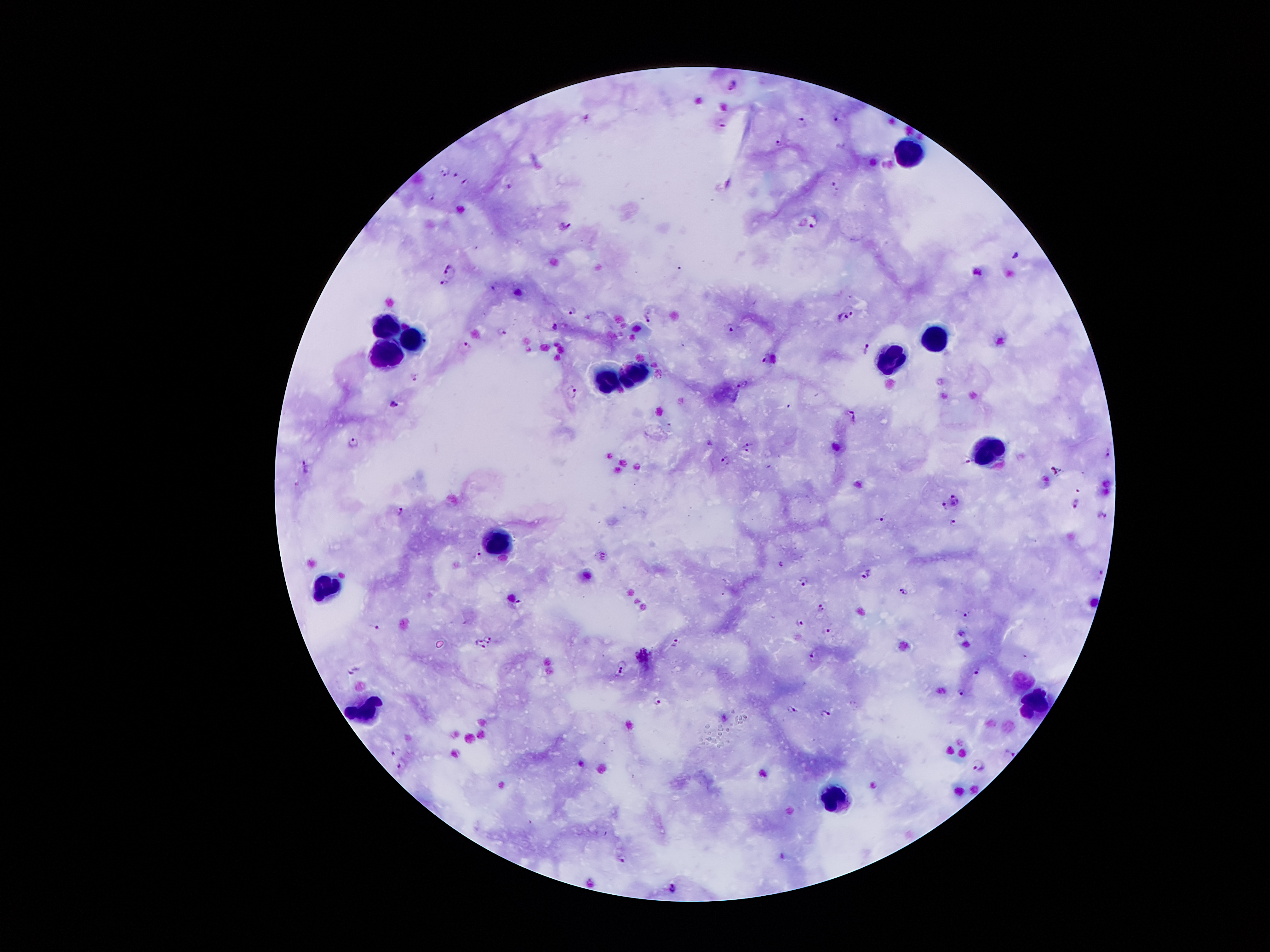
{
  "image_size": "1270×952 pixels",
  "patient_malaria_status": "infected with Plasmodium falciparum",
  "preparation": "thick blood film",
  "magnification": "100x",
  "field_of_view": "single",
  "leukocyte_locations": "approximate centers as [x, y] in pixels: [906, 152], [391, 324], [418, 336], [934, 338], [390, 354], [887, 357], [636, 371], [611, 380], [992, 446], [502, 539], [330, 584], [1023, 680], [1037, 702], [367, 710], [836, 796]",
  "malaria_parasite_locations": "approximate centers as [x, y] in pixels: [734, 84], [836, 116], [799, 120], [722, 123], [778, 145], [440, 171], [452, 172], [463, 180], [506, 182], [834, 183], [435, 195], [812, 221], [564, 224], [1017, 256], [448, 269], [443, 284], [851, 308], [572, 310], [842, 316], [647, 317], [555, 324], [731, 326], [501, 329], [465, 342], [867, 345], [766, 356], [414, 373], [741, 384], [571, 389], [393, 402], [852, 413], [353, 441], [748, 444], [707, 445], [1109, 453], [726, 460], [967, 462], [306, 467], [955, 499], [1076, 502], [944, 508], [401, 510], [1103, 515], [882, 518], [953, 523], [477, 554], [868, 575], [1101, 575], [804, 579], [904, 591], [518, 601], [822, 607], [966, 615], [801, 623], [375, 625], [827, 628], [490, 636], [674, 642], [483, 645], [643, 654], [1026, 656], [810, 657], [624, 662], [353, 669], [977, 670], [618, 673], [961, 691], [657, 701], [792, 708], [826, 711], [394, 752], [1010, 754], [403, 765], [979, 765], [622, 859], [673, 888]",
  "capture": "smartphone camera through the microscope eyepiece",
  "stain": "Giemsa"
}